Point out each leukocyte.
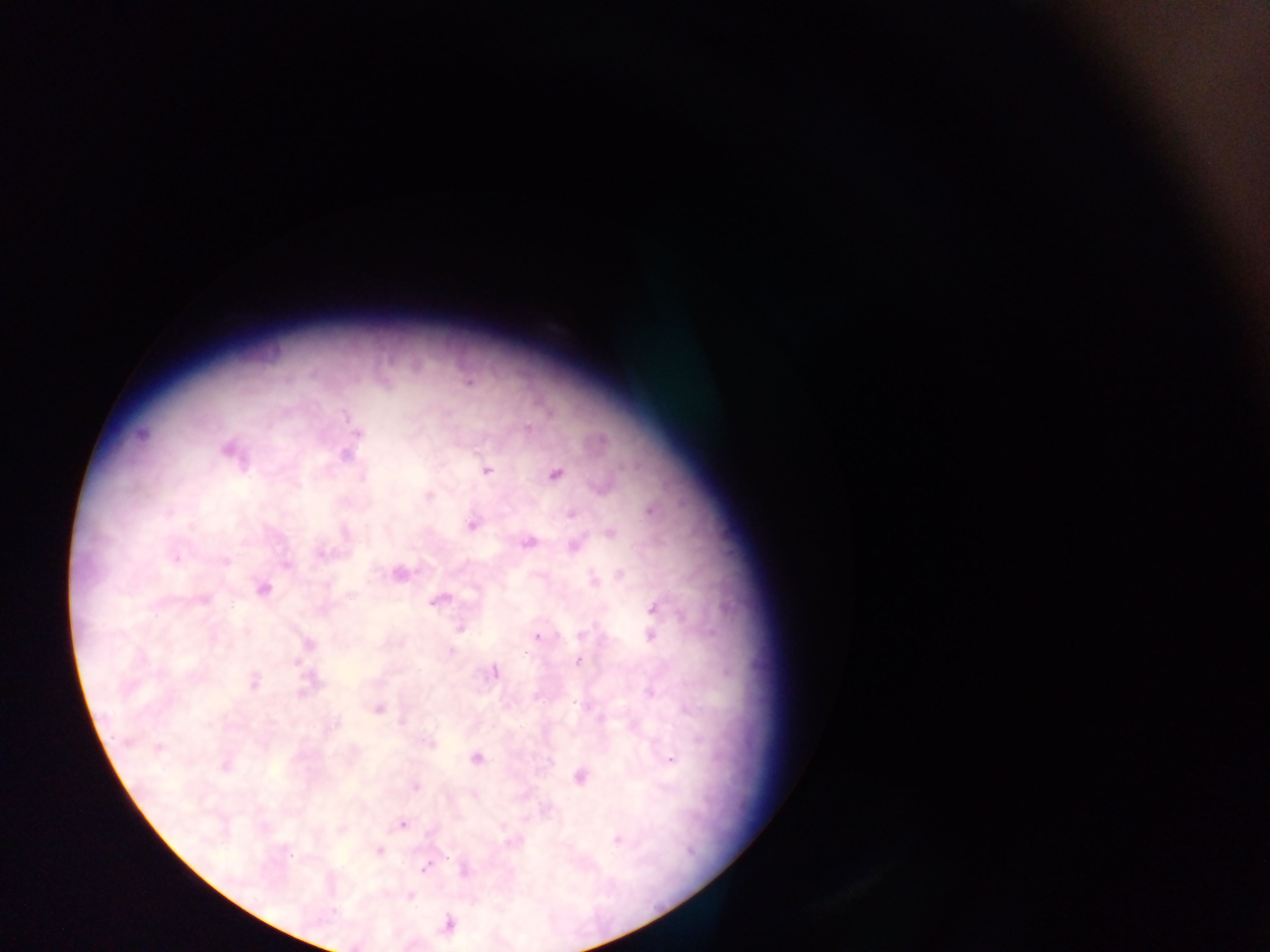

No leukocytes observed.

Approximate centers as (x, y) in pixels.
Summary:
  - Malaria parasite locations: (469, 382), (345, 415), (528, 428), (357, 433), (141, 434), (226, 450), (345, 456), (488, 470), (554, 474), (362, 476), (429, 496), (651, 510), (573, 515), (472, 525), (191, 527), (610, 533), (528, 543), (574, 547), (321, 553), (175, 559), (225, 562), (286, 565), (401, 574), (620, 574), (594, 580), (263, 589), (204, 600), (438, 601), (655, 609), (461, 629), (582, 634), (651, 636), (537, 637), (308, 644), (451, 650), (579, 661), (495, 673), (254, 683), (651, 692), (577, 704), (378, 709), (335, 723), (430, 743), (158, 747), (476, 759), (670, 760), (225, 767), (580, 777), (416, 786), (402, 825), (617, 840), (379, 850), (290, 855), (425, 868), (410, 896), (449, 924)
  - Preparation: thick blood smear
  - Image size: 1270×952 pixels
  - Field of view: single
  - Capture: mobile-phone photograph through a microscope
  - Country: Ghana